Classify this cell by malaria status.
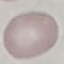
It is uninfected.

capture = smartphone camera at the microscope eyepiece
stain = Giemsa
preparation = thin blood film
image type = cell patch, automatically extracted from a larger field of view and resized to 64 × 64 pixels